Classify this cell by malaria status.
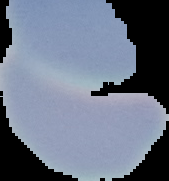

Uninfected.

{
  "preparation": "thin blood film",
  "image_type": "segmented cell region on a black background",
  "image_size": "169×181 pixels"
}